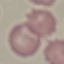
result = no malaria parasites seen
image type = cell patch, automatically extracted from a larger field of view and resized to 64 × 64 pixels
capture = smartphone camera at the microscope eyepiece
preparation = thin blood smear
stain = Giemsa